Outline each blood parasite and name the species.
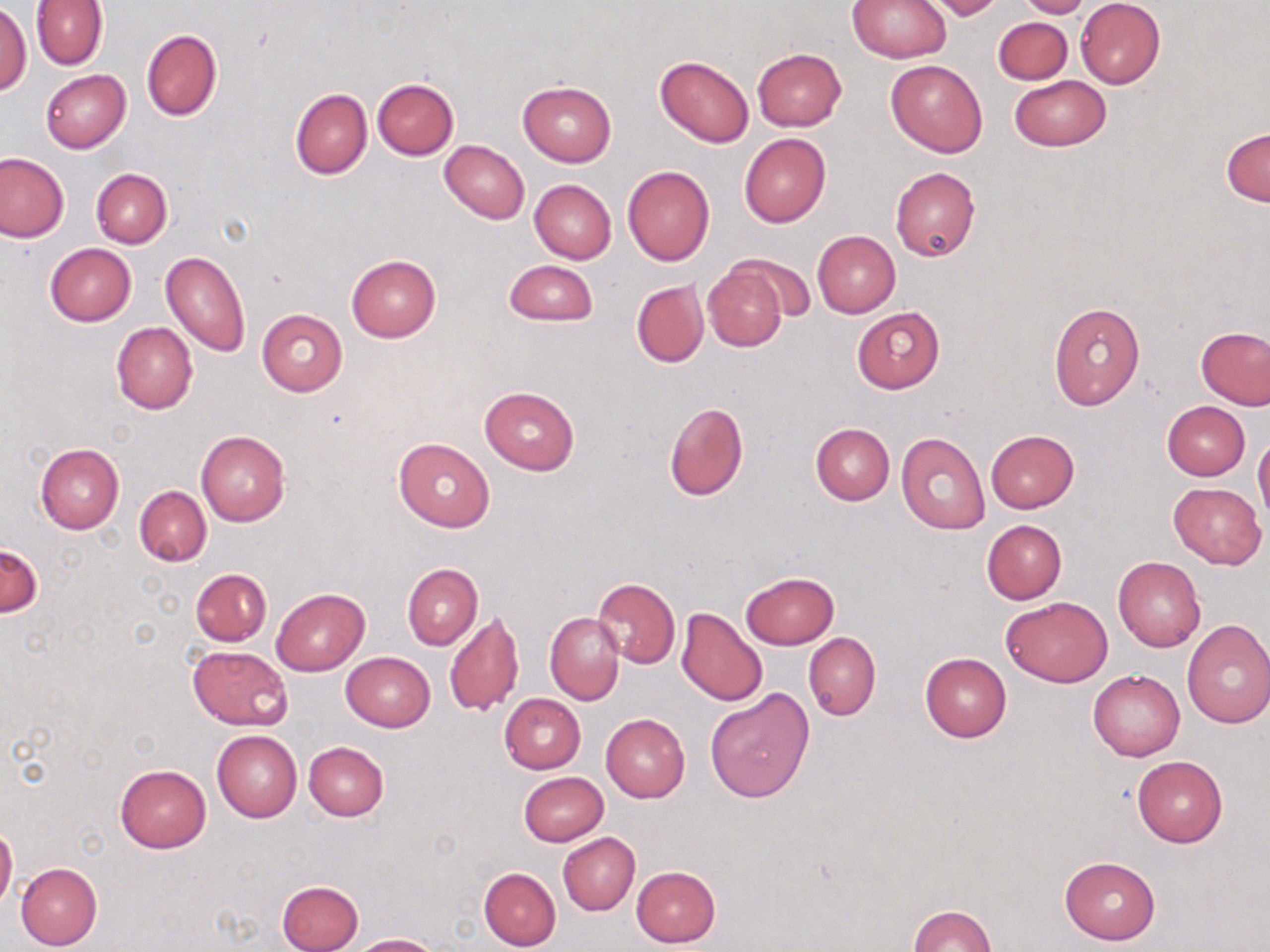
No blood parasites seen.

slide-level diagnosis = negative for blood parasites
uninfected red blood cell locations = approximate bounding boxes as (x1,y1)-(x2,y2) corner pairs in pixels: (848,0)-(950,62), (923,0)-(1004,21), (1014,0)-(1092,18), (30,1)-(108,70), (1074,1)-(1166,88), (0,5)-(31,97), (993,17)-(1072,85), (140,28)-(223,122), (752,48)-(847,131), (655,55)-(755,148), (886,59)-(987,157), (40,69)-(130,152), (1009,76)-(1111,151), (372,79)-(459,160), (517,81)-(616,165), (289,88)-(371,179), (1222,127)-(1270,206), (738,132)-(831,227), (439,140)-(529,224), (0,152)-(68,242), (623,166)-(716,266), (891,167)-(980,262), (91,168)-(172,248), (529,179)-(616,263), (812,231)-(901,317), (45,242)-(137,325), (160,251)-(251,357), (346,254)-(440,341), (732,254)-(816,321), (504,260)-(597,327), (702,260)-(790,352), (631,280)-(708,367), (1048,302)-(1145,410), (851,306)-(945,392), (257,308)-(347,396), (111,322)-(197,414), (1196,326)-(1270,410), (480,385)-(579,475), (663,400)-(749,502), (1162,401)-(1250,480), (810,423)-(893,505), (196,430)-(289,528), (985,430)-(1080,513), (896,431)-(991,534), (393,437)-(494,532), (1253,437)-(1270,523), (36,443)-(124,533), (1168,483)-(1265,568), (135,486)-(211,566), (982,519)-(1067,603), (0,542)-(41,616), (1113,556)-(1205,651), (401,563)-(482,651), (190,568)-(272,645), (741,571)-(838,649), (593,577)-(680,669), (272,588)-(369,675), (1001,596)-(1111,688), (677,606)-(768,707), (445,609)-(523,717), (545,612)-(623,705), (1181,619)-(1270,728), (803,632)-(880,720), (188,645)-(292,730), (341,652)-(436,731), (920,653)-(1012,742), (1088,669)-(1185,760), (705,690)-(814,804), (499,693)-(584,774), (601,713)-(689,802), (211,729)-(301,821), (303,742)-(388,821), (1132,754)-(1228,847), (114,764)-(211,853), (519,771)-(608,846), (0,824)-(17,910), (558,833)-(640,916), (1059,856)-(1160,945), (15,862)-(102,950), (631,866)-(721,947), (479,867)-(561,949), (277,880)-(363,952), (908,905)-(996,952), (350,933)-(437,951)
modality = optical microscopy
stain = May-Grünwald-Giemsa
magnification = 1000x
image size = 1270×952 pixels
preparation = thin blood smear
field of view = single